Report the malaria status of this cell.
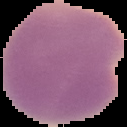
It is parasitized.

Cell region segmented out of the field of view; the surrounding area is masked to black. Image is 127×127 pixels. From a thin blood smear.